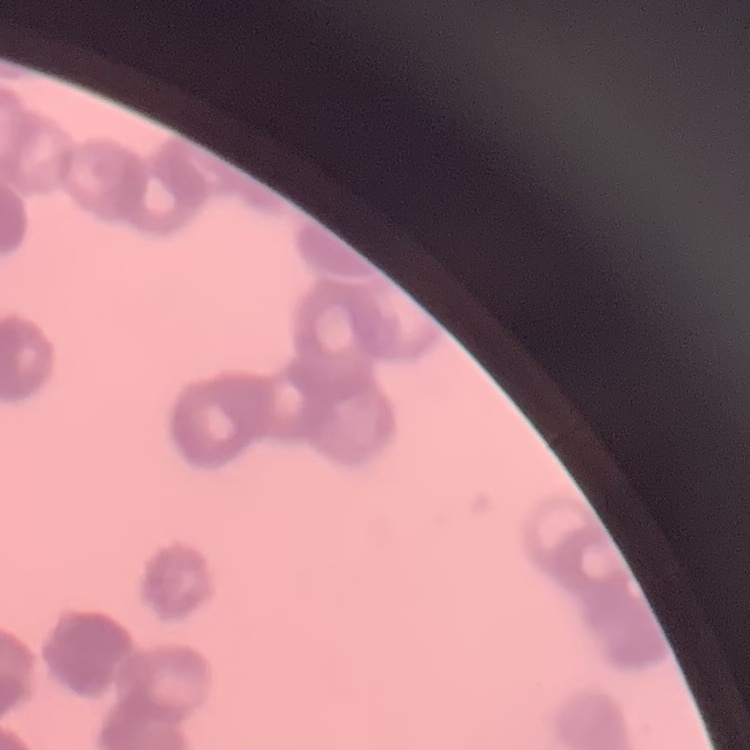 The red blood cells show rouleaux formation. Thin blood film. Stained with either Field's or Giemsa. One tile cut from a larger photomicrograph.